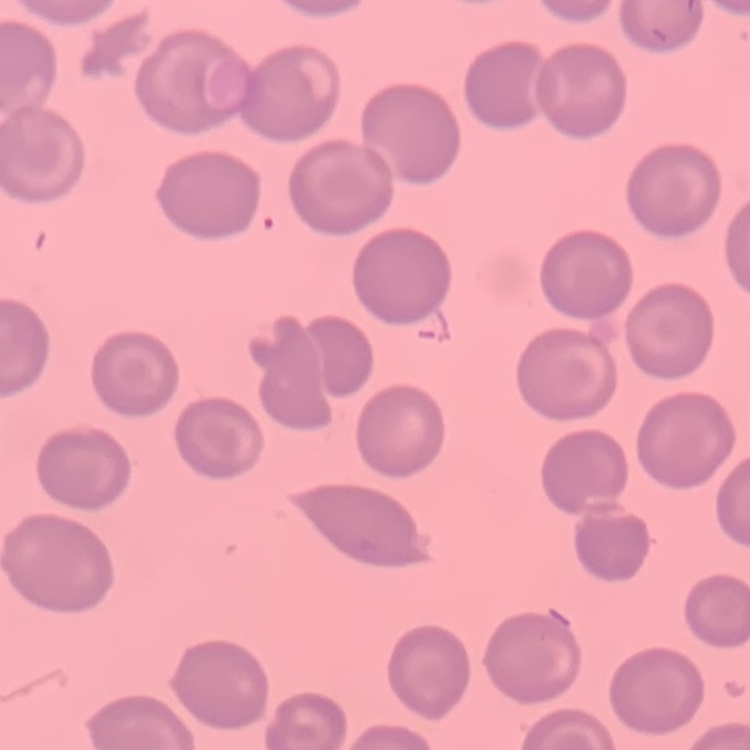
{
  "red_blood_cell_morphology": "no rouleaux formation",
  "image_type": "one tile cut from a larger photomicrograph",
  "preparation": "thin peripheral smear",
  "stain": "Field's or Giemsa"
}